State which parasite is depicted.
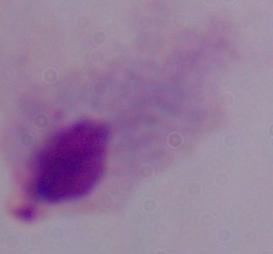

A trichomonad.

modality: photomicrograph
magnification: 1000x